State which parasite is depicted.
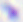

This is Toxoplasma gondii.

Summary:
  - Modality: micrograph
  - Magnification: 400x